Classify this cell by malaria status.
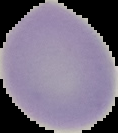

Uninfected.

From a thin blood film. Segmented cell region on a black background. Image is 118×133 pixels.